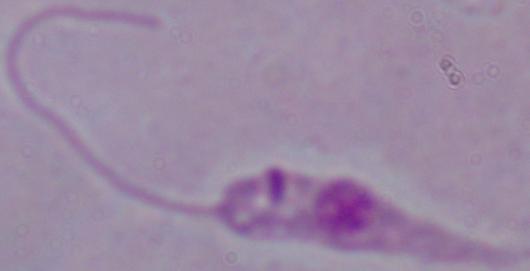
{
  "modality": "micrograph",
  "identification": "Leishmania",
  "magnification": "1000x"
}